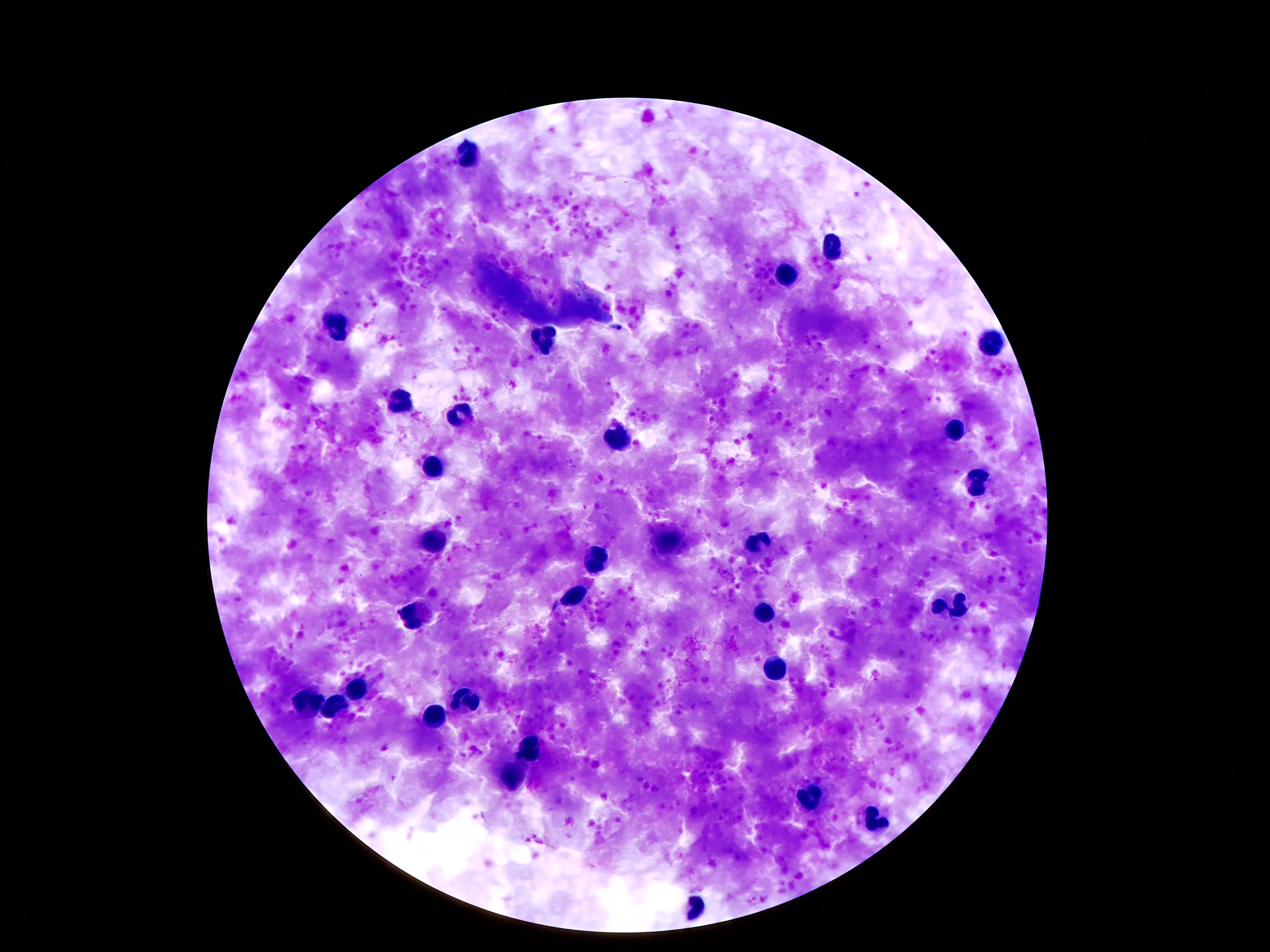

Approximate centers as (x, y) in pixels.
Summary:
  - Leukocyte locations: (471, 152), (833, 247), (790, 274), (342, 324), (545, 340), (993, 342), (402, 402), (463, 416), (956, 432), (616, 437), (435, 460), (976, 485), (435, 542), (665, 544), (760, 544), (596, 559), (575, 595), (952, 600), (764, 615), (415, 617), (775, 666), (355, 690), (465, 701), (312, 702), (338, 705), (428, 718), (529, 746), (519, 780), (812, 798), (876, 821), (700, 908)
  - Stain: Giemsa
  - Capture: smartphone camera through the microscope eyepiece
  - Patient malaria status: not infected
  - Magnification: 100x
  - Image size: 1270×952 pixels
  - Preparation: thick blood smear
  - Field of view: single